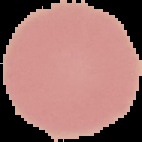
Image is 142×142 pixels. From a thin blood film. The area outside the segmented cell region is set to black. Malaria status: uninfected.